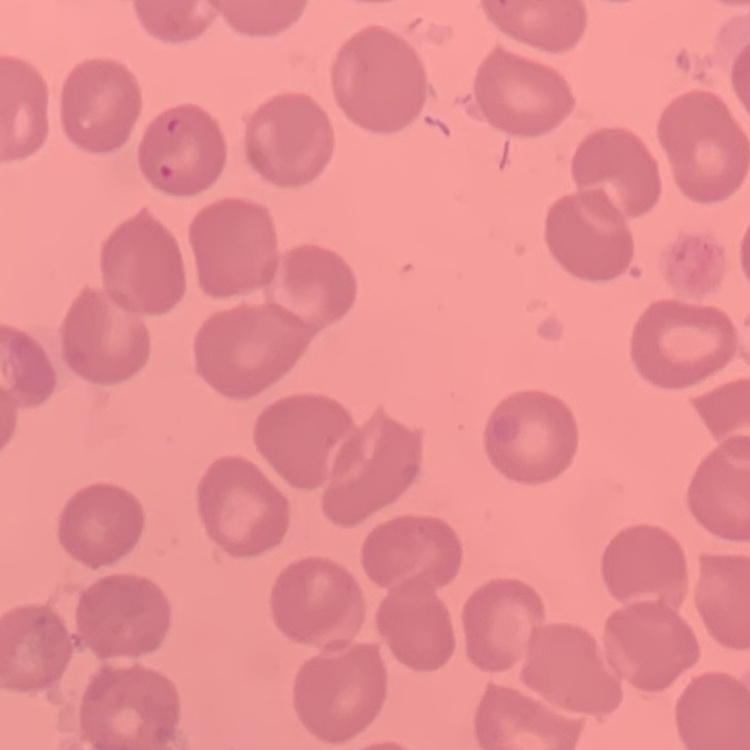
erythrocyte morphology = no rouleaux formation
preparation = thin peripheral smear
stain = Field's or Giemsa
image type = square crop of a larger photomicrograph